Assess this cell for malaria.
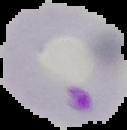
Parasitized.

Summary:
  - Preparation: thin blood smear
  - Image type: cell region segmented out of the field of view; surrounding area masked to black
  - Image size: 127×130 pixels